Locate every Plasmodium parasite and identify its life-cycle stage.
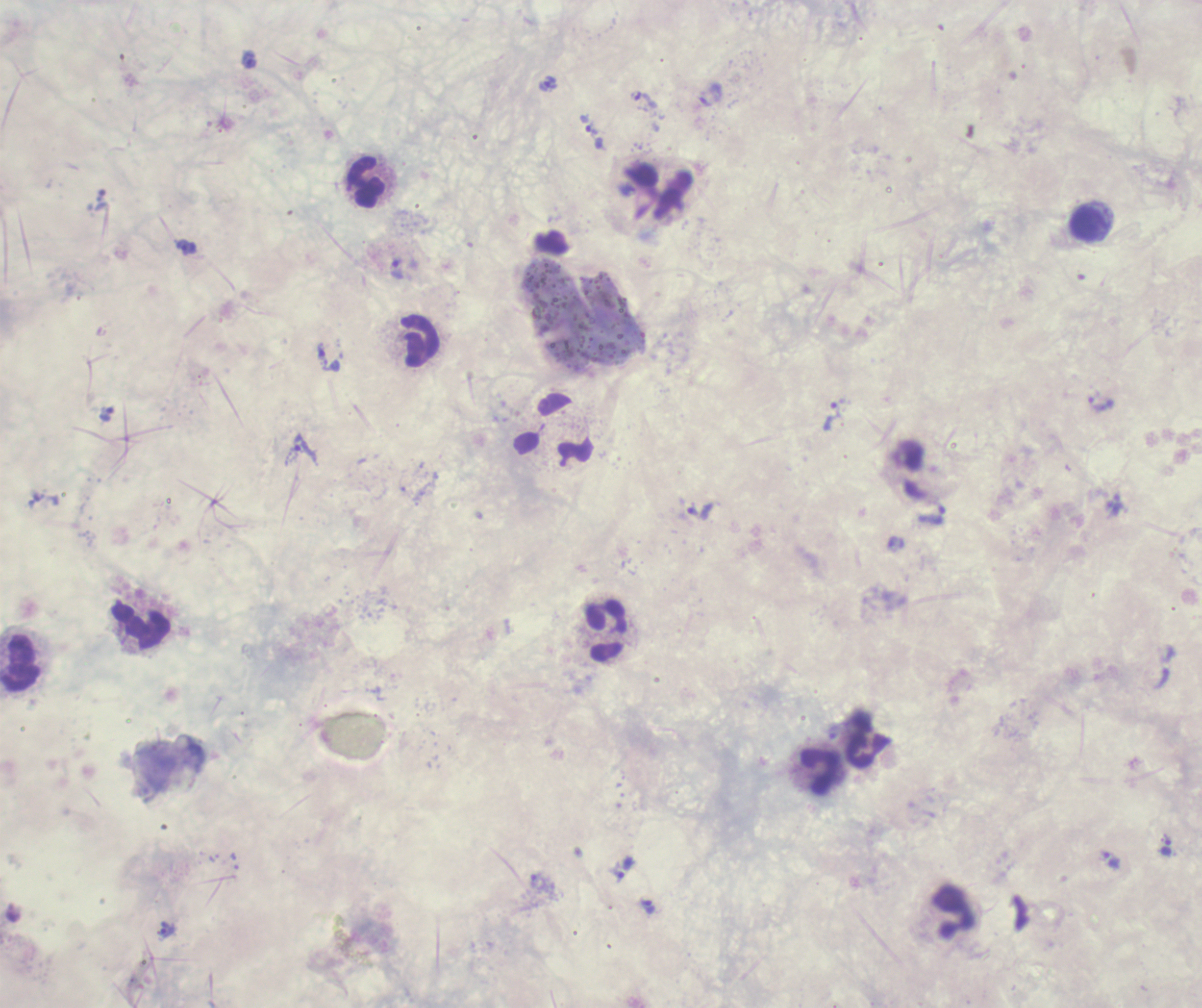

Approximate centers as [x, y] in pixels.
Trophozoites: [249, 60], [548, 83], [645, 100], [594, 136], [186, 247], [397, 269], [327, 361], [1101, 405], [107, 414], [831, 416], [305, 449], [700, 511], [931, 517], [1166, 848], [1111, 861], [623, 868], [650, 907], [167, 929].
No schizont or gametocyte forms observed.

Approximate centers as [x, y] in pixels.
Summary:
  - Leukocyte locations: [366, 182], [1089, 225], [420, 341], [140, 626], [606, 631], [20, 663], [867, 739], [819, 771]
  - Magnification: 100x
  - Context: previously used in an actual diagnosis
  - Coloration quality: bad
  - Image size: 1202×1008 pixels
  - Background quality: poor
  - Field of view: one from this slide
  - Stain: Romanowsky
  - Preparation: thick smear of blood